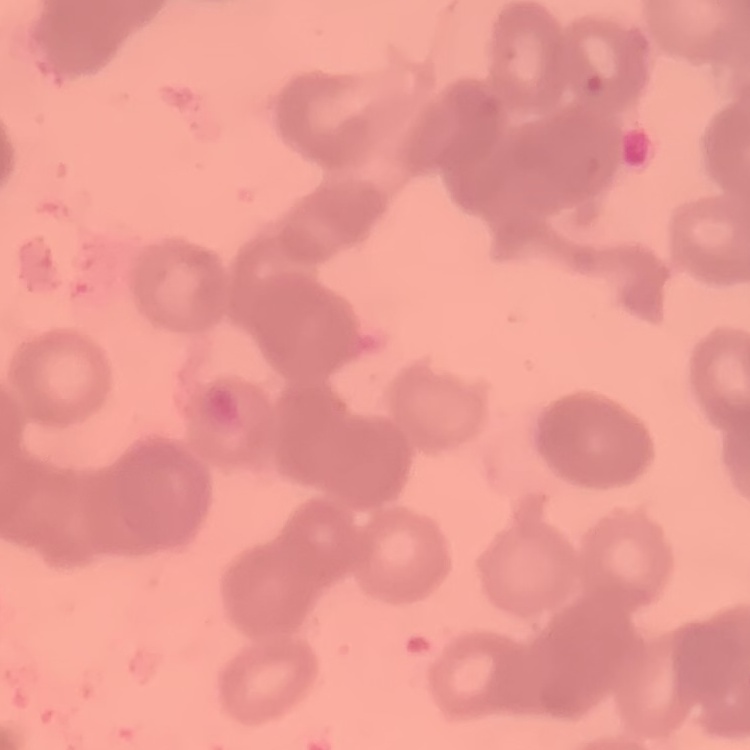
Summary:
  - Erythrocyte morphology: rouleaux formation
  - Image type: one tile cut from a larger photomicrograph
  - Preparation: thin peripheral smear
  - Stain: Field's or Giemsa